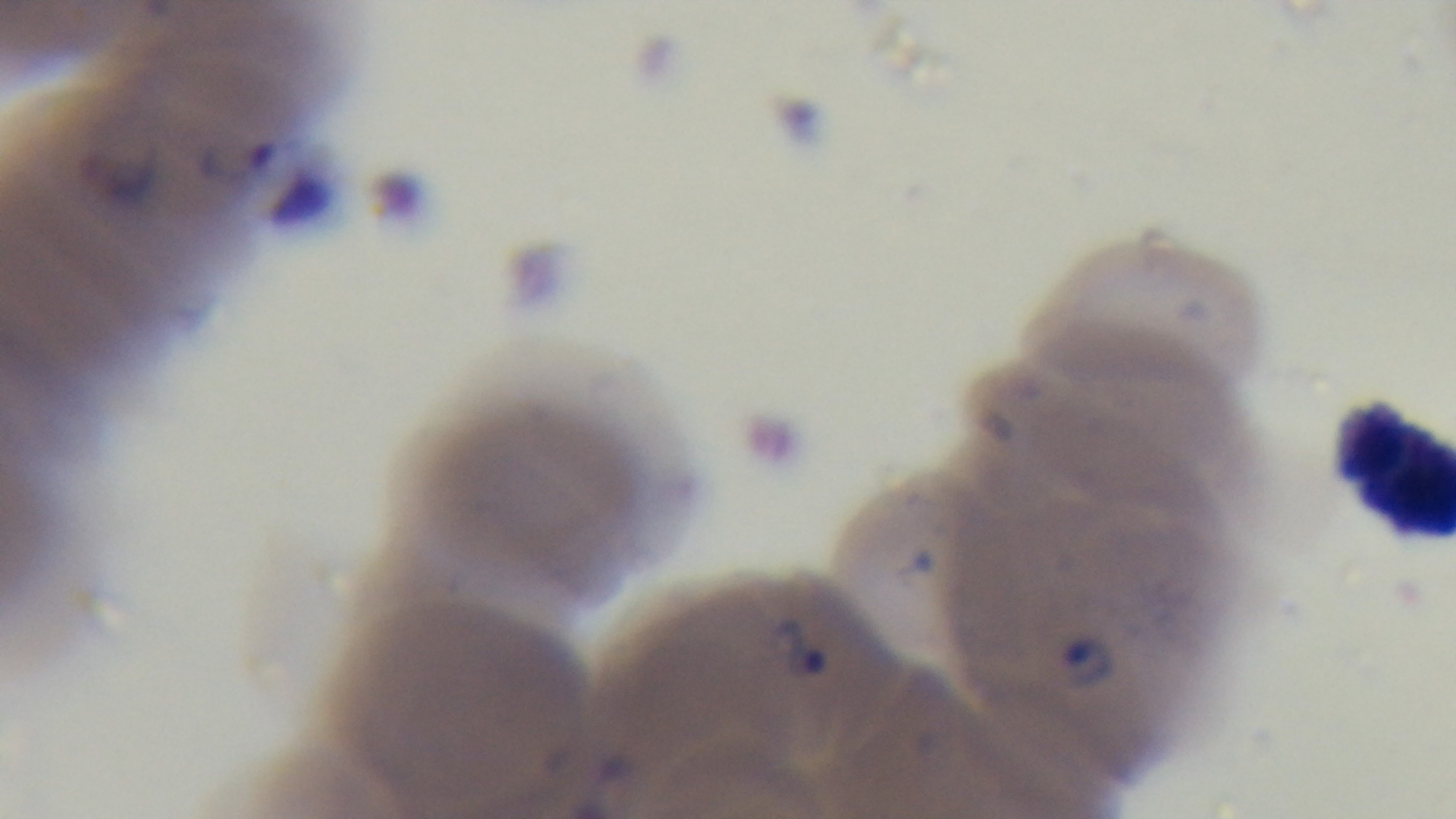

preparation = thin
modality = light microscopy
capture = mounted 4K digital camera
objective = 100x oil immersion
stain = Giemsa
malaria status = infected
field of view = one from the slide